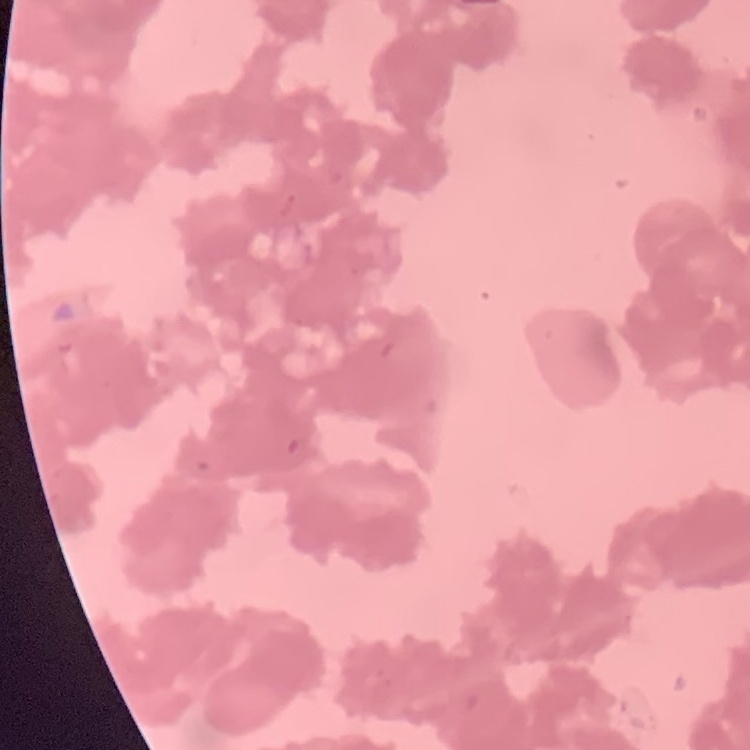

red blood cell morphology = rouleaux formation
preparation = thin peripheral smear
image type = square crop of a larger photomicrograph
stain = Field's or Giemsa